Assess the morphology of the erythrocytes.
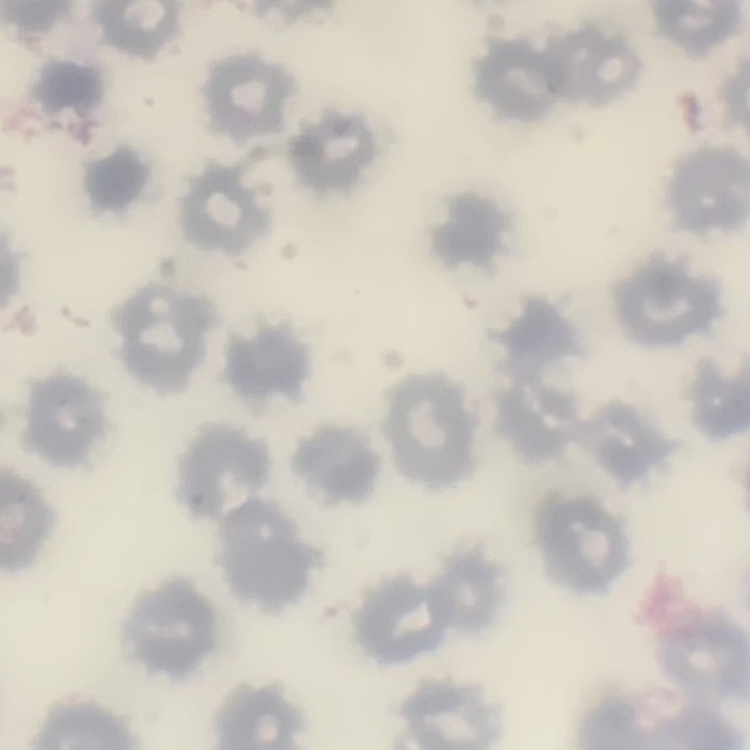

No rouleaux formation.

{
  "stain": "Field's or Giemsa",
  "image_type": "square crop of a larger photomicrograph",
  "preparation": "thin blood smear"
}